Report the malaria status of this cell.
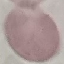

It is uninfected.

preparation = thin blood film
image type = cell patch, automatically extracted from a larger field of view and resized to 64 × 64 pixels
capture = smartphone camera at the microscope eyepiece
stain = Giemsa